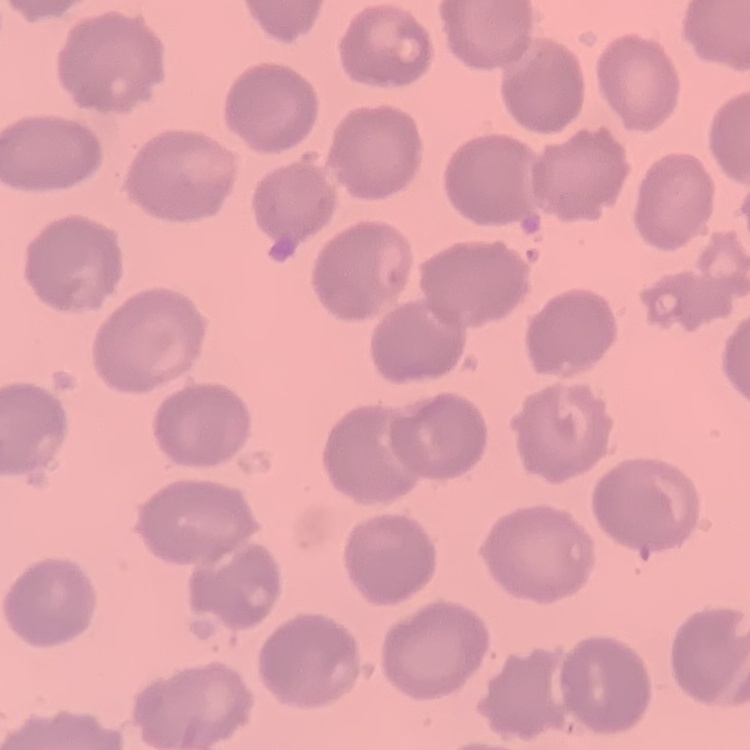
Summary:
  - Red blood cell morphology: no rouleaux formation
  - Stain: Field's or Giemsa
  - Preparation: thin blood smear
  - Image type: square crop of a larger photomicrograph